Name the blood parasite species.
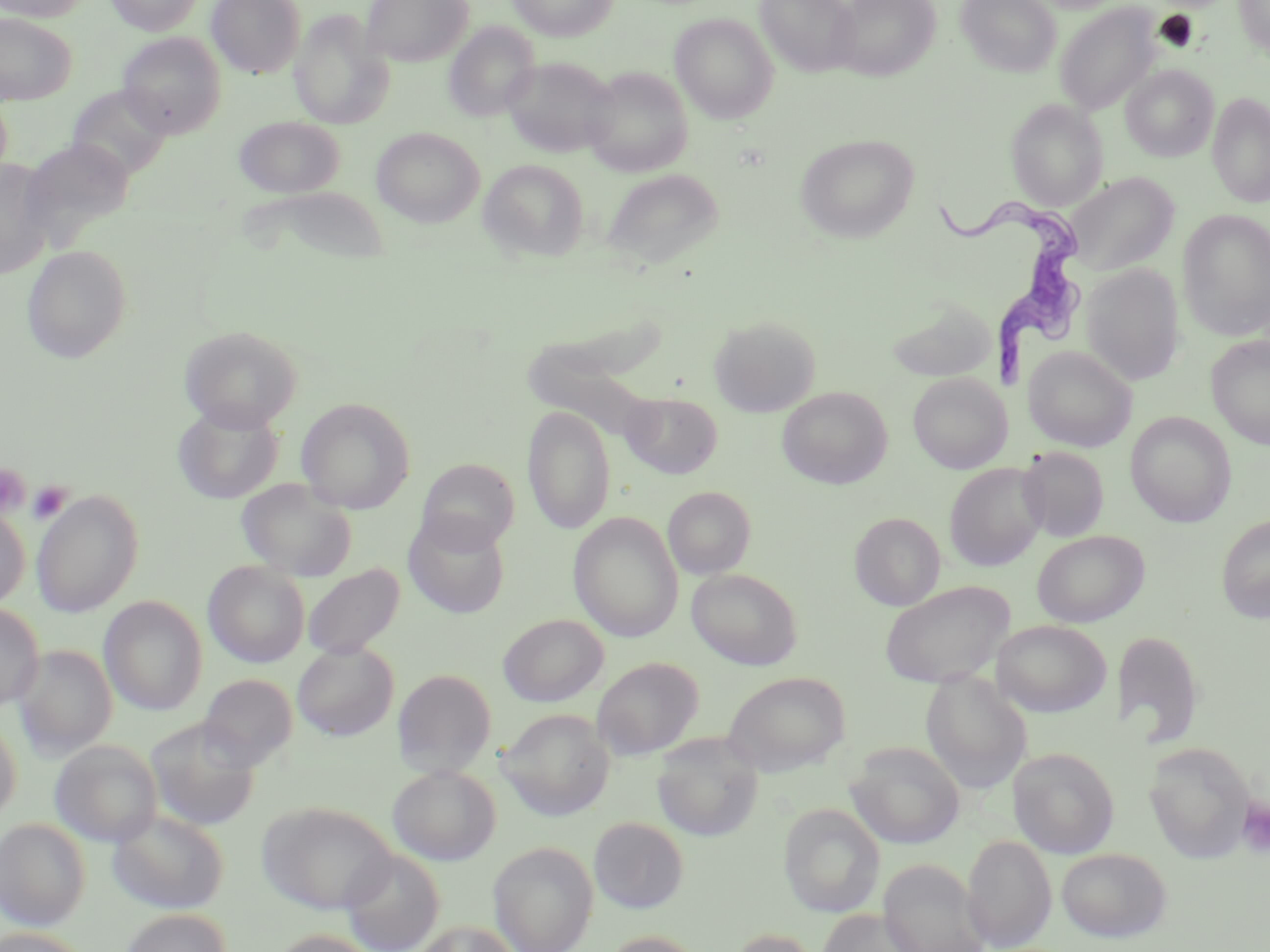
Trypanosoma brucei.

Summary:
  - Coordinate format: approximate bounding boxes as (x1,y1)-(x2,y2) corner pairs in pixels
  - Platelet locations: (1,465)-(31,518), (27,481)-(72,524), (1236,796)-(1270,858)
  - Trypanosoma brucei locations: (935,189)-(1087,375)
  - Uninfected red blood cell locations: (0,0)-(93,22), (105,0)-(204,35), (207,0)-(305,78), (361,0)-(472,66), (507,0)-(619,41), (755,0)-(860,76), (831,0)-(940,81), (956,0)-(1061,76), (1234,0)-(1270,59), (1054,3)-(1162,115), (288,9)-(393,130), (0,13)-(75,104), (670,13)-(779,123), (444,22)-(540,122), (118,32)-(227,138), (500,56)-(618,158), (1121,65)-(1219,162), (582,66)-(694,177), (66,86)-(172,179), (1208,92)-(1270,207), (1006,99)-(1108,210), (234,116)-(344,198), (372,126)-(484,227), (797,134)-(919,242), (22,137)-(136,243), (478,158)-(589,262), (0,160)-(57,279), (601,168)-(724,269), (1063,172)-(1179,277), (243,186)-(394,267), (1177,209)-(1270,341), (22,244)-(133,363), (1081,263)-(1185,386), (884,296)-(997,383), (709,315)-(821,417), (178,325)-(303,431), (1206,336)-(1270,449), (1023,346)-(1136,452), (908,372)-(1012,473), (778,387)-(891,489), (621,391)-(723,479), (296,397)-(416,514), (172,403)-(283,504), (522,406)-(615,535), (1125,412)-(1236,527), (1018,447)-(1109,542), (417,458)-(520,554), (945,462)-(1047,571), (236,478)-(356,582), (663,486)-(755,579), (32,489)-(144,617), (0,506)-(30,610), (569,512)-(683,643), (403,513)-(510,619), (849,513)-(946,610), (1216,514)-(1270,622), (1032,530)-(1149,627), (203,560)-(310,668), (302,563)-(404,660), (687,568)-(802,670), (880,581)-(1015,688), (100,596)-(207,716), (0,602)-(43,712), (498,614)-(608,707), (991,620)-(1111,717), (1112,629)-(1205,748), (292,641)-(399,741), (13,645)-(117,759), (592,657)-(703,759), (392,669)-(497,777), (921,670)-(1032,793), (723,672)-(850,776), (199,674)-(297,771), (497,709)-(615,820), (0,715)-(21,823), (145,717)-(260,831), (652,733)-(763,841), (50,740)-(162,847), (847,741)-(965,849), (1144,743)-(1254,862), (1008,747)-(1120,858), (387,764)-(500,865), (257,800)-(397,914), (778,803)-(884,917), (107,807)-(229,914), (589,817)-(689,913), (0,818)-(90,930), (962,834)-(1056,950), (488,841)-(598,952), (1056,847)-(1173,943), (339,848)-(445,952), (877,858)-(990,952), (817,908)-(928,952), (118,909)-(233,952), (414,920)-(521,952), (0,927)-(92,952), (726,928)-(823,952), (268,929)-(384,952), (599,930)-(708,952)
  - Field of view: single
  - Preparation: thin blood smear
  - Stain: May-Grünwald-Giemsa
  - Modality: optical microscopy
  - Image size: 1270×952 pixels
  - Magnification: 1000x